Give the extent of all Plasmodium ovale-infected red blood cells.
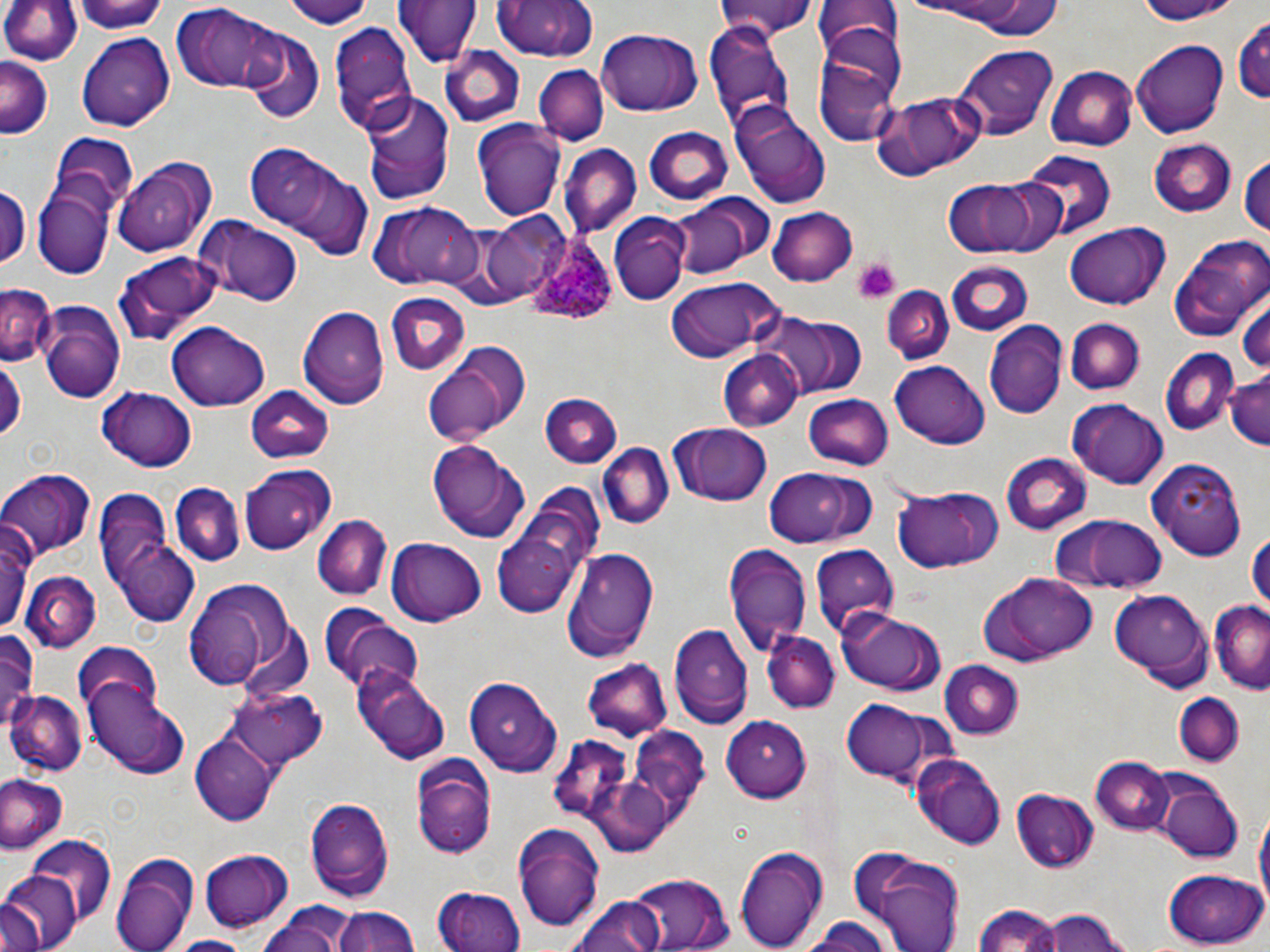
Approximate bounding boxes as named x1/y1/x2/y2 corners in pixels.
Plasmodium ovale-infected red blood cells: (x1=522, y1=231, x2=618, y2=325).

Summary:
  - Platelet locations: (x1=853, y1=258, x2=901, y2=304)
  - Uninfected red blood cell locations: (x1=1, y1=0, x2=83, y2=67), (x1=75, y1=0, x2=171, y2=35), (x1=278, y1=0, x2=375, y2=28), (x1=393, y1=0, x2=483, y2=69), (x1=490, y1=0, x2=600, y2=63), (x1=713, y1=0, x2=817, y2=39), (x1=893, y1=0, x2=1063, y2=28), (x1=1128, y1=0, x2=1244, y2=24), (x1=811, y1=1, x2=901, y2=57), (x1=172, y1=2, x2=288, y2=95), (x1=1233, y1=12, x2=1270, y2=110), (x1=328, y1=22, x2=416, y2=134), (x1=707, y1=22, x2=795, y2=125), (x1=813, y1=28, x2=903, y2=141), (x1=599, y1=29, x2=702, y2=115), (x1=242, y1=30, x2=325, y2=122), (x1=76, y1=34, x2=174, y2=131), (x1=1130, y1=40, x2=1229, y2=139), (x1=441, y1=44, x2=525, y2=128), (x1=958, y1=46, x2=1056, y2=135), (x1=0, y1=57, x2=54, y2=138), (x1=534, y1=66, x2=606, y2=145), (x1=1045, y1=67, x2=1136, y2=152), (x1=358, y1=89, x2=455, y2=207), (x1=871, y1=91, x2=987, y2=182), (x1=735, y1=108, x2=832, y2=207), (x1=473, y1=121, x2=563, y2=222), (x1=645, y1=128, x2=734, y2=205), (x1=47, y1=132, x2=138, y2=215), (x1=242, y1=140, x2=373, y2=258), (x1=1148, y1=140, x2=1238, y2=219), (x1=561, y1=143, x2=641, y2=238), (x1=1023, y1=154, x2=1115, y2=240), (x1=1239, y1=154, x2=1269, y2=239), (x1=112, y1=159, x2=214, y2=259), (x1=940, y1=177, x2=1053, y2=258), (x1=0, y1=186, x2=29, y2=271), (x1=32, y1=187, x2=115, y2=279), (x1=669, y1=193, x2=772, y2=280), (x1=366, y1=202, x2=482, y2=290), (x1=770, y1=206, x2=856, y2=285), (x1=610, y1=214, x2=690, y2=305), (x1=198, y1=219, x2=300, y2=307), (x1=457, y1=220, x2=553, y2=306), (x1=1064, y1=223, x2=1168, y2=310), (x1=1166, y1=230, x2=1266, y2=342), (x1=112, y1=253, x2=219, y2=345), (x1=945, y1=262, x2=1035, y2=337), (x1=664, y1=278, x2=783, y2=363), (x1=1, y1=287, x2=56, y2=368), (x1=881, y1=288, x2=952, y2=365), (x1=1237, y1=290, x2=1270, y2=377), (x1=386, y1=294, x2=469, y2=375), (x1=39, y1=302, x2=124, y2=401), (x1=299, y1=307, x2=388, y2=410), (x1=773, y1=314, x2=866, y2=396), (x1=1064, y1=318, x2=1143, y2=395), (x1=166, y1=323, x2=272, y2=410), (x1=984, y1=323, x2=1065, y2=420), (x1=422, y1=343, x2=531, y2=447), (x1=1158, y1=348, x2=1240, y2=437), (x1=719, y1=350, x2=805, y2=431), (x1=0, y1=358, x2=25, y2=440), (x1=889, y1=361, x2=990, y2=449), (x1=1225, y1=369, x2=1270, y2=452), (x1=244, y1=387, x2=335, y2=465), (x1=98, y1=389, x2=197, y2=472), (x1=803, y1=393, x2=894, y2=471), (x1=540, y1=394, x2=622, y2=469), (x1=1067, y1=398, x2=1170, y2=488), (x1=670, y1=423, x2=772, y2=507), (x1=426, y1=440, x2=530, y2=543), (x1=600, y1=443, x2=673, y2=529), (x1=1001, y1=453, x2=1092, y2=535), (x1=1149, y1=456, x2=1247, y2=557), (x1=239, y1=464, x2=334, y2=553), (x1=759, y1=467, x2=865, y2=548), (x1=0, y1=469, x2=96, y2=559), (x1=167, y1=480, x2=246, y2=570), (x1=489, y1=482, x2=606, y2=616), (x1=889, y1=485, x2=1003, y2=573), (x1=92, y1=490, x2=178, y2=599), (x1=1047, y1=513, x2=1166, y2=595), (x1=313, y1=515, x2=391, y2=600), (x1=0, y1=517, x2=33, y2=639), (x1=1245, y1=526, x2=1270, y2=618), (x1=110, y1=534, x2=202, y2=627), (x1=387, y1=538, x2=485, y2=626), (x1=725, y1=545, x2=811, y2=659), (x1=811, y1=545, x2=899, y2=639), (x1=563, y1=548, x2=659, y2=663), (x1=20, y1=573, x2=100, y2=653), (x1=976, y1=573, x2=1099, y2=665), (x1=180, y1=577, x2=297, y2=688), (x1=1109, y1=588, x2=1214, y2=688), (x1=1210, y1=598, x2=1270, y2=693), (x1=322, y1=607, x2=422, y2=695), (x1=837, y1=608, x2=948, y2=697), (x1=670, y1=623, x2=751, y2=730), (x1=0, y1=630, x2=41, y2=732), (x1=763, y1=631, x2=839, y2=714), (x1=72, y1=642, x2=164, y2=726), (x1=582, y1=658, x2=672, y2=742), (x1=935, y1=659, x2=1024, y2=739), (x1=353, y1=667, x2=452, y2=766), (x1=464, y1=675, x2=562, y2=776), (x1=84, y1=686, x2=189, y2=779), (x1=227, y1=687, x2=327, y2=771), (x1=6, y1=692, x2=85, y2=776), (x1=1174, y1=693, x2=1246, y2=765), (x1=842, y1=701, x2=932, y2=781), (x1=721, y1=716, x2=814, y2=799), (x1=633, y1=725, x2=711, y2=801), (x1=193, y1=731, x2=276, y2=825), (x1=545, y1=736, x2=626, y2=813), (x1=911, y1=753, x2=1008, y2=848), (x1=412, y1=755, x2=496, y2=859), (x1=1091, y1=757, x2=1175, y2=835), (x1=0, y1=771, x2=68, y2=856), (x1=1155, y1=780, x2=1244, y2=863), (x1=591, y1=781, x2=667, y2=856), (x1=1012, y1=789, x2=1099, y2=873), (x1=304, y1=797, x2=393, y2=902), (x1=1253, y1=804, x2=1269, y2=924), (x1=513, y1=822, x2=606, y2=931), (x1=25, y1=837, x2=117, y2=931), (x1=734, y1=843, x2=831, y2=950), (x1=847, y1=845, x2=969, y2=951), (x1=199, y1=849, x2=295, y2=933), (x1=112, y1=850, x2=200, y2=952), (x1=1163, y1=868, x2=1267, y2=948), (x1=0, y1=871, x2=78, y2=952), (x1=624, y1=875, x2=735, y2=950), (x1=435, y1=888, x2=526, y2=952), (x1=568, y1=894, x2=667, y2=952), (x1=973, y1=902, x2=1066, y2=951), (x1=258, y1=903, x2=356, y2=952), (x1=333, y1=904, x2=419, y2=952), (x1=1036, y1=907, x2=1138, y2=951), (x1=798, y1=918, x2=899, y2=952), (x1=165, y1=934, x2=251, y2=952)
  - Slide-level diagnosis: Plasmodium ovale
  - Field of view: single
  - Image size: 1270×952 pixels
  - Preparation: thin blood smear
  - Stain: May-Grünwald-Giemsa
  - Magnification: 1000x
  - Modality: light microscopy